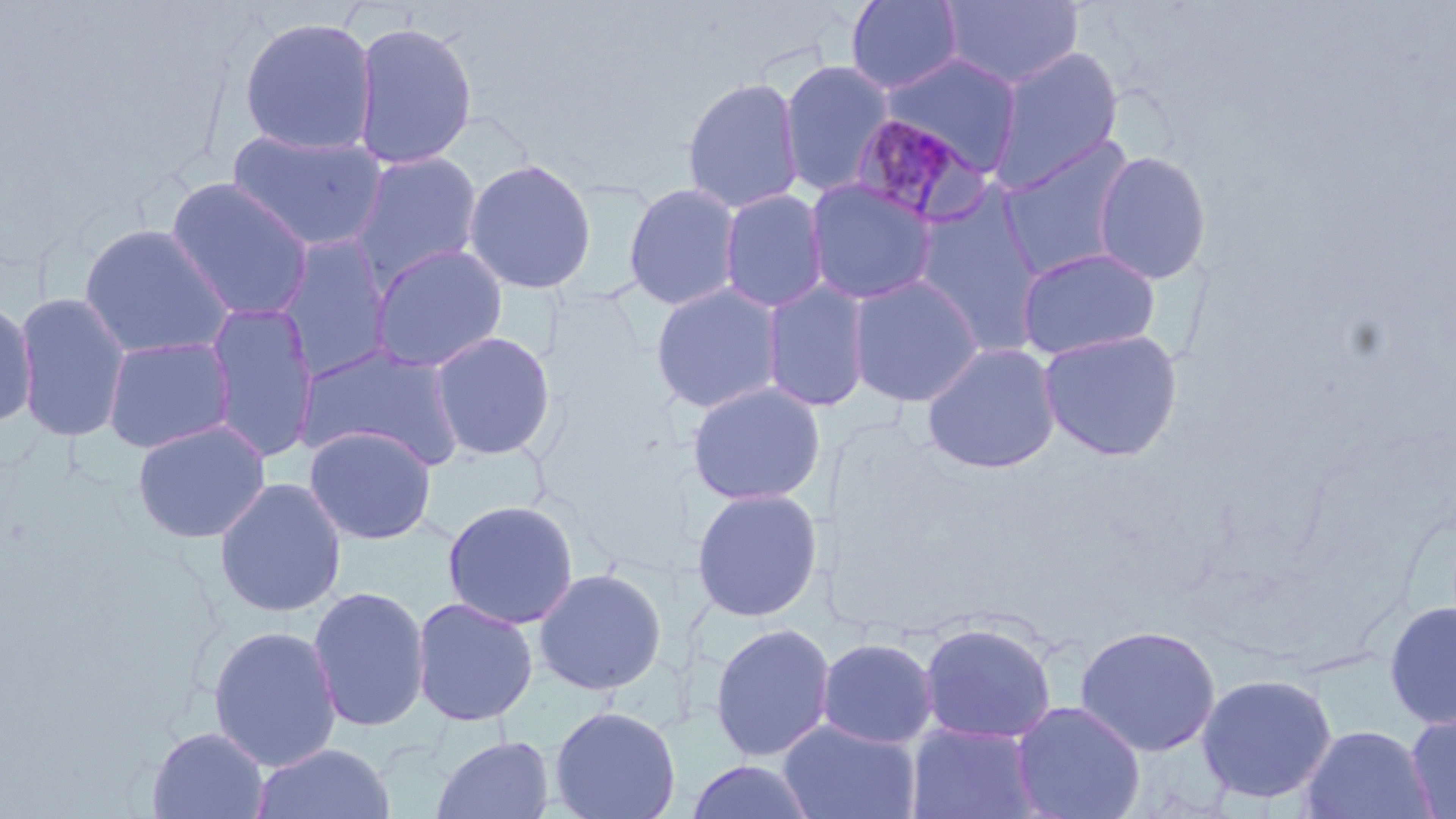

Summary:
  - Coordinate format: approximate bounding boxes as [x1, y1, x2, y2] in pixels
  - Uninfected red blood cell locations: [844, 0, 965, 94], [940, 0, 1085, 90], [237, 16, 378, 157], [351, 21, 477, 170], [990, 46, 1123, 190], [878, 52, 1023, 175], [777, 60, 896, 197], [681, 76, 804, 214], [226, 129, 389, 253], [995, 134, 1140, 281], [347, 150, 484, 287], [1091, 150, 1213, 285], [462, 157, 598, 294], [165, 177, 315, 322], [804, 178, 938, 306], [623, 183, 742, 311], [718, 189, 830, 314], [910, 189, 1048, 355], [78, 223, 234, 362], [272, 234, 395, 380], [369, 243, 509, 373], [1014, 246, 1161, 362], [846, 274, 985, 408], [760, 279, 872, 413], [650, 282, 784, 415], [13, 292, 132, 443], [0, 299, 37, 428], [204, 302, 320, 463], [1037, 328, 1184, 462], [429, 331, 556, 461], [102, 335, 236, 454], [921, 341, 1062, 474], [296, 342, 466, 473], [686, 381, 826, 507], [131, 420, 271, 544], [303, 425, 437, 545], [213, 477, 347, 618], [690, 488, 824, 622], [441, 499, 580, 630], [533, 567, 668, 696], [307, 585, 431, 733], [409, 589, 670, 717], [411, 596, 539, 727], [1383, 600, 1456, 728], [708, 622, 836, 762], [918, 622, 1057, 743], [207, 624, 343, 771], [1074, 624, 1223, 757], [816, 637, 939, 748], [1196, 672, 1338, 804], [1010, 700, 1146, 819], [549, 704, 681, 819], [1405, 712, 1456, 818], [778, 720, 922, 819], [905, 722, 1042, 819], [1299, 724, 1437, 819], [146, 727, 270, 818], [431, 734, 555, 819], [250, 742, 396, 819], [685, 760, 819, 819]
  - Plasmodium malariae-infected red blood cell locations: [846, 110, 990, 227]
  - Slide-level diagnosis: Plasmodium malariae
  - Magnification: 1000x
  - Image size: 1456×819 pixels
  - Stain: May-Grünwald-Giemsa
  - Preparation: thin blood smear
  - Modality: optical microscopy
  - Field of view: one of a larger specimen